Give the location of every white blood cell.
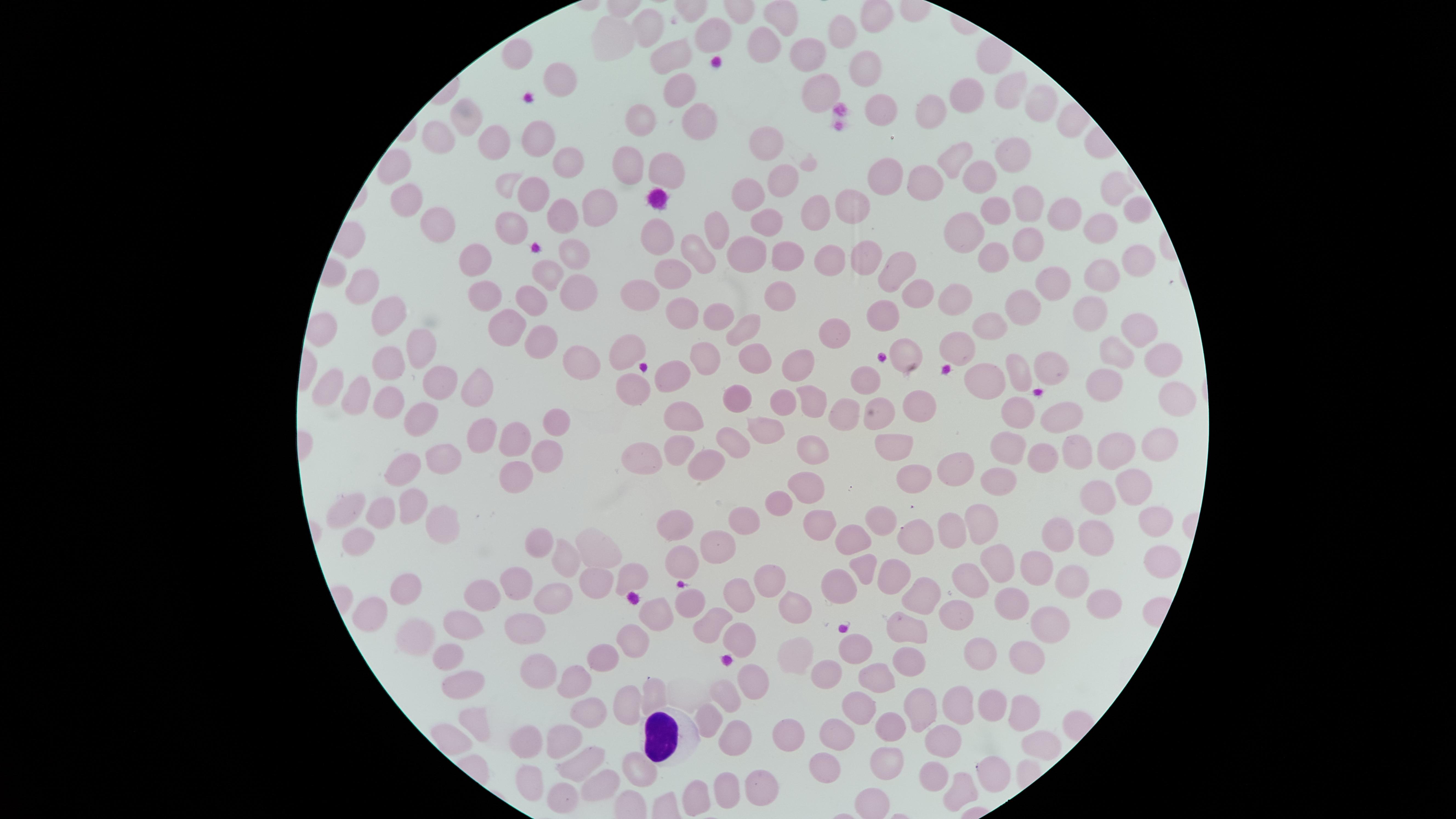

Approximate marker points, in pixels from the top-left corner.
White blood cells: (x=666, y=740).

Approximate marker points, in pixels from the top-left corner. Uninfected red blood cells: (x=781, y=16), (x=648, y=24), (x=840, y=29), (x=708, y=32), (x=614, y=35), (x=761, y=42), (x=672, y=55), (x=803, y=55), (x=518, y=58), (x=862, y=63), (x=557, y=77), (x=675, y=86), (x=815, y=88), (x=1006, y=93), (x=963, y=96), (x=1037, y=104), (x=928, y=106), (x=469, y=115), (x=875, y=115), (x=689, y=117), (x=640, y=120), (x=434, y=134), (x=536, y=136), (x=768, y=141), (x=491, y=143), (x=958, y=151), (x=1014, y=154), (x=569, y=156), (x=657, y=160), (x=621, y=161), (x=781, y=172), (x=915, y=176), (x=980, y=176), (x=879, y=179), (x=1109, y=189), (x=529, y=190), (x=747, y=194), (x=408, y=196), (x=1026, y=203), (x=995, y=205), (x=591, y=207), (x=846, y=209), (x=1131, y=209), (x=813, y=210), (x=1063, y=210), (x=556, y=214), (x=441, y=220), (x=507, y=221), (x=967, y=222), (x=763, y=223), (x=1098, y=223), (x=720, y=231), (x=658, y=239), (x=1021, y=241), (x=744, y=250), (x=565, y=254), (x=699, y=254), (x=781, y=255), (x=991, y=255), (x=476, y=257), (x=830, y=259), (x=1137, y=259), (x=860, y=261), (x=896, y=270), (x=1101, y=272), (x=673, y=273), (x=542, y=274), (x=1050, y=274), (x=359, y=279), (x=921, y=287), (x=639, y=289), (x=481, y=292), (x=569, y=292), (x=778, y=294), (x=954, y=295), (x=1022, y=298), (x=530, y=302), (x=385, y=304), (x=684, y=310), (x=1091, y=312), (x=719, y=315), (x=881, y=316), (x=500, y=324), (x=984, y=324), (x=741, y=330), (x=1135, y=330), (x=828, y=334), (x=949, y=339), (x=417, y=341), (x=532, y=343), (x=626, y=346), (x=910, y=348), (x=1118, y=348), (x=704, y=350), (x=752, y=351), (x=1157, y=353), (x=569, y=358), (x=799, y=360), (x=390, y=362), (x=1048, y=363), (x=1018, y=367), (x=667, y=372), (x=987, y=377), (x=333, y=381), (x=434, y=381), (x=476, y=381), (x=866, y=381), (x=1098, y=383), (x=636, y=388), (x=355, y=395), (x=390, y=397), (x=807, y=397), (x=1173, y=397), (x=782, y=398), (x=920, y=398), (x=736, y=399), (x=1013, y=409), (x=879, y=410), (x=688, y=411), (x=847, y=411), (x=418, y=412), (x=1057, y=417), (x=552, y=418), (x=757, y=421), (x=479, y=432), (x=513, y=436), (x=727, y=438), (x=1158, y=438), (x=1004, y=444), (x=674, y=445), (x=1114, y=445), (x=895, y=446), (x=1071, y=447), (x=1040, y=449), (x=640, y=450), (x=545, y=452), (x=810, y=452), (x=452, y=458), (x=953, y=465), (x=410, y=466), (x=520, y=472), (x=992, y=477), (x=906, y=480), (x=804, y=485), (x=1131, y=487), (x=1101, y=497), (x=410, y=502), (x=352, y=506), (x=778, y=506), (x=384, y=511), (x=878, y=517), (x=979, y=517), (x=818, y=518), (x=1145, y=518), (x=434, y=519), (x=744, y=523), (x=682, y=525), (x=948, y=531), (x=1058, y=532), (x=917, y=534), (x=1091, y=535), (x=858, y=537), (x=540, y=538), (x=357, y=541), (x=720, y=543), (x=599, y=545), (x=567, y=556), (x=992, y=558), (x=1157, y=558), (x=682, y=566), (x=1033, y=568), (x=860, y=569), (x=890, y=573), (x=632, y=576), (x=766, y=576), (x=592, y=579), (x=1068, y=579), (x=521, y=582), (x=963, y=582), (x=836, y=583), (x=402, y=585), (x=919, y=591), (x=550, y=595), (x=737, y=596), (x=485, y=599), (x=1012, y=599), (x=1103, y=600), (x=686, y=601), (x=796, y=601), (x=650, y=607), (x=953, y=608), (x=364, y=612), (x=712, y=616), (x=1045, y=620), (x=906, y=624), (x=525, y=625), (x=455, y=629), (x=407, y=630), (x=726, y=631), (x=628, y=642), (x=800, y=647), (x=852, y=647), (x=986, y=652), (x=444, y=656), (x=904, y=656), (x=1023, y=656), (x=602, y=660), (x=536, y=669), (x=828, y=674), (x=874, y=676), (x=458, y=678), (x=578, y=679), (x=745, y=679), (x=643, y=694), (x=721, y=699), (x=992, y=703), (x=926, y=704), (x=960, y=708), (x=588, y=710), (x=620, y=710), (x=850, y=711), (x=1021, y=714), (x=473, y=721), (x=710, y=721), (x=883, y=728), (x=567, y=729), (x=834, y=730), (x=525, y=733), (x=793, y=736), (x=732, y=739), (x=1037, y=740), (x=942, y=742), (x=577, y=761), (x=886, y=763), (x=823, y=766), (x=994, y=767), (x=937, y=770), (x=638, y=771), (x=526, y=777), (x=596, y=777), (x=764, y=785), (x=959, y=786), (x=728, y=788), (x=559, y=793), (x=698, y=798). Image is 1456×819 pixels. The visible region is circular. Presence: no malaria parasites detected. One field of view of the specimen. Thin blood smear. Photographed with a smartphone camera through the microscope eyepiece. Giemsa-stained preparation.